Classify this cell by malaria status.
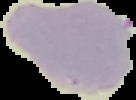
Uninfected.

Image is 136×100 pixels. From a thin blood film. The area outside the segmented cell region is set to black.